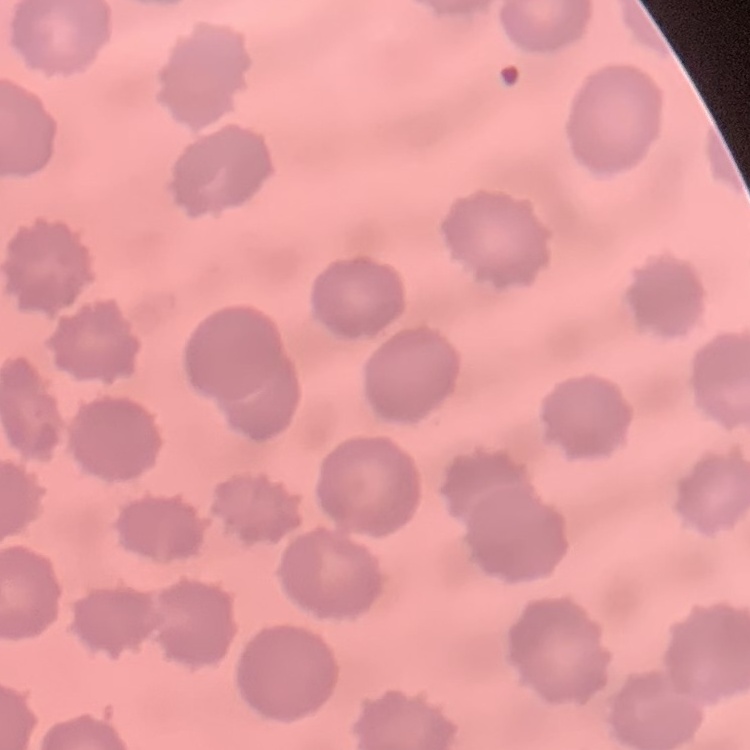

Summary:
  - Red blood cell morphology: no rouleaux formation
  - Image type: one tile cut from a larger photomicrograph
  - Preparation: thin blood film
  - Stain: Field's or Giemsa